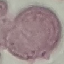

Summary:
  - Malaria status: uninfected
  - Stain: Giemsa
  - Image type: automatically extracted cell patch, resized to 64 × 64 pixels
  - Capture: smartphone through the microscope eyepiece
  - Preparation: thin blood film